State the blood parasite species.
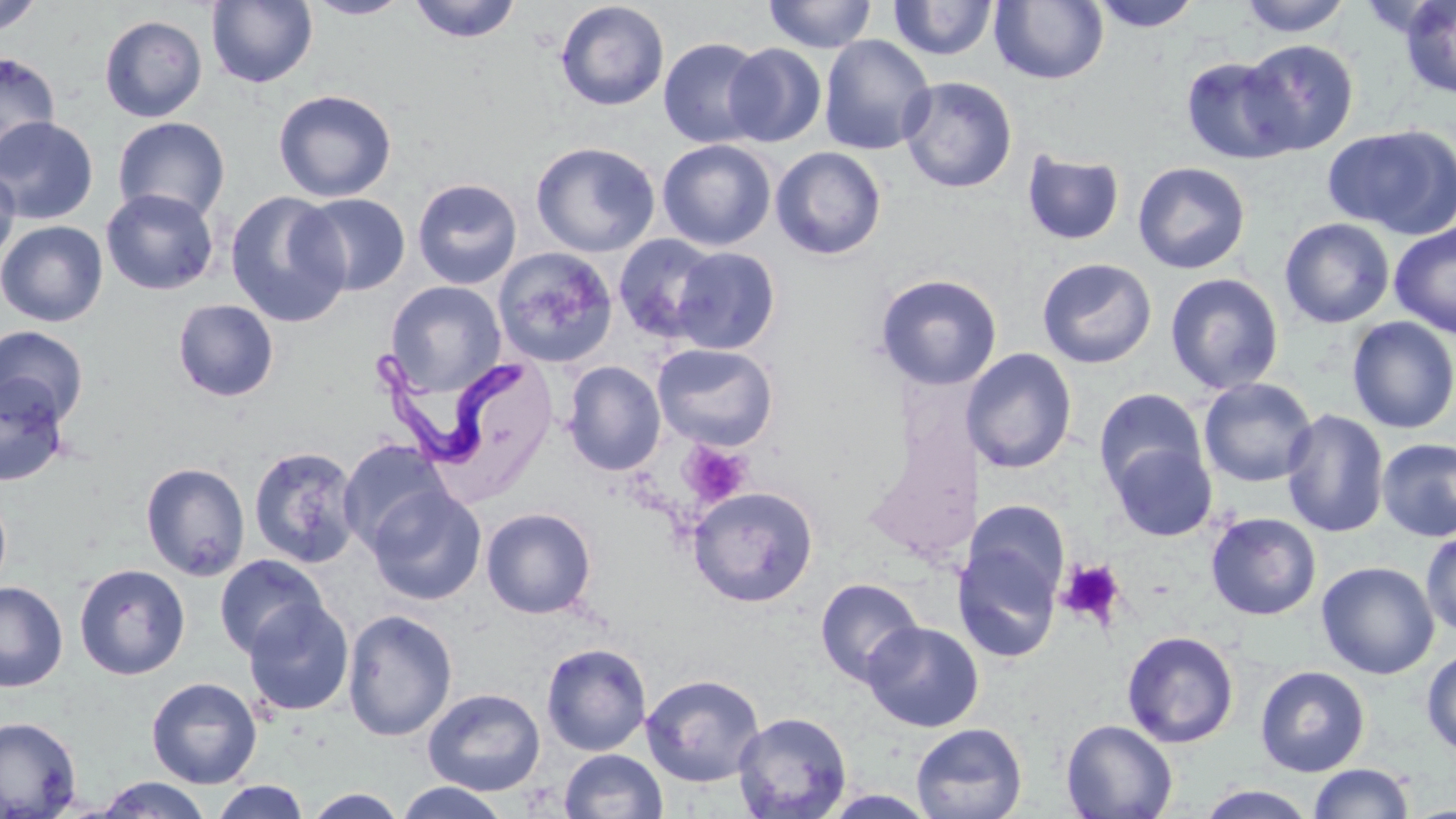

Trypanosoma brucei.

Summary:
  - Coordinate format: approximate bounding boxes as (x1,y1)-(x2,y2) corner pairs in pixels
  - Uninfected red blood cell locations: (0,0)-(44,36), (303,0)-(412,20), (408,0)-(522,43), (763,0)-(878,53), (1089,0)-(1203,32), (1235,0)-(1353,38), (1398,0)-(1456,100), (206,1)-(318,88), (554,1)-(670,111), (888,1)-(1000,62), (989,1)-(1109,85), (99,14)-(207,122), (818,34)-(936,155), (658,37)-(768,148), (1240,40)-(1359,154), (723,43)-(827,147), (0,52)-(60,166), (1180,55)-(1303,164), (897,76)-(1018,194), (272,89)-(397,203), (0,116)-(98,224), (112,117)-(230,224), (1323,124)-(1456,237), (657,139)-(777,251), (531,141)-(661,258), (770,146)-(887,260), (1021,149)-(1126,246), (1133,161)-(1251,274), (0,165)-(20,267), (412,178)-(523,289), (101,188)-(219,295), (224,191)-(351,328), (296,192)-(411,296), (1279,217)-(1395,328), (0,220)-(108,327), (1389,222)-(1456,339), (613,234)-(724,342), (670,246)-(781,354), (493,247)-(618,368), (1036,257)-(1157,369), (1164,272)-(1284,395), (875,273)-(1002,390), (385,281)-(506,396), (172,298)-(279,402), (1346,316)-(1456,434), (0,326)-(89,426), (652,342)-(779,451), (962,348)-(1078,473), (562,360)-(666,475), (0,374)-(70,487), (1198,377)-(1318,488), (1093,387)-(1207,495), (1281,409)-(1389,537), (1376,437)-(1456,543), (338,439)-(453,555), (1108,440)-(1218,542), (247,446)-(362,568), (140,462)-(251,581), (366,485)-(487,606), (687,485)-(819,608), (0,488)-(12,597), (973,500)-(1070,605), (481,507)-(597,619), (1206,512)-(1322,620), (1421,530)-(1456,637), (954,541)-(1062,664), (214,554)-(329,659), (1317,560)-(1440,679), (74,563)-(191,680), (815,577)-(924,686), (0,581)-(68,692), (242,598)-(354,717), (342,609)-(458,742), (862,621)-(984,732), (1122,630)-(1239,748), (541,642)-(652,756), (1421,647)-(1455,758), (1254,665)-(1370,776), (641,674)-(765,787), (146,676)-(262,788), (423,687)-(547,796), (733,711)-(852,819), (0,716)-(82,818), (1061,718)-(1178,819), (911,722)-(1027,819), (560,749)-(668,819), (1309,763)-(1414,819), (95,776)-(213,818), (209,780)-(310,818), (393,781)-(511,818), (1196,784)-(1317,819), (302,788)-(409,818), (820,790)-(940,818)
  - Platelet locations: (680,442)-(751,507), (1057,559)-(1126,628)
  - Trypanosoma brucei locations: (371,349)-(534,466)
  - Preparation: thin blood film
  - Stain: May-Grünwald-Giemsa
  - Magnification: 1000x
  - Field of view: single
  - Image size: 1456×819 pixels
  - Modality: light microscopy